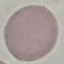
Summary:
  - Result: negative for malaria parasites
  - Stain: Giemsa
  - Preparation: thin blood smear
  - Capture: smartphone camera at the microscope eyepiece
  - Image type: automatically extracted cell patch, resized to 64 × 64 pixels